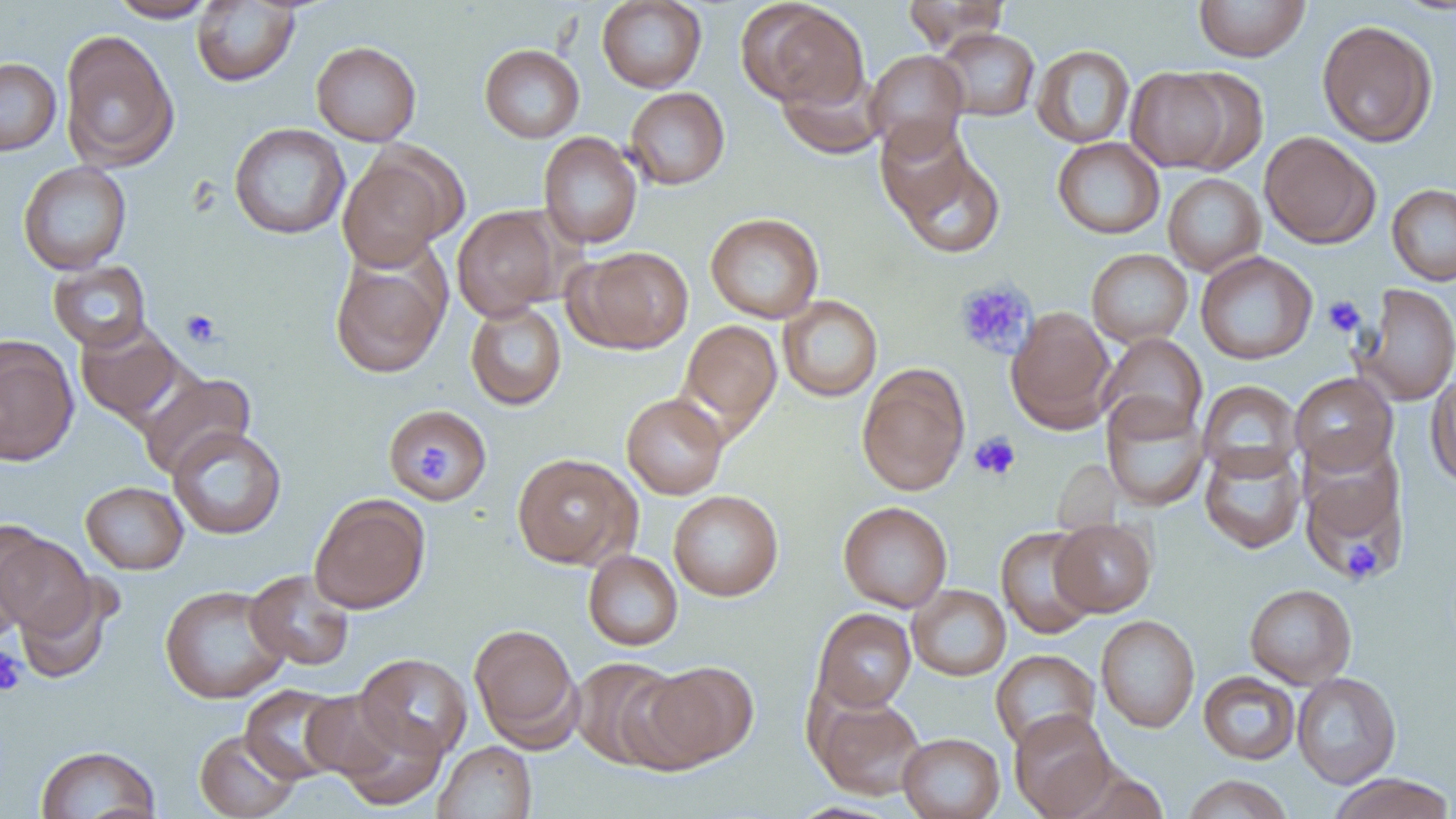
Approximate bounding boxes as [x1, y1, x2, y2] in pixels. Uninfected red blood cell locations: [108, 0, 219, 22], [597, 0, 707, 93], [902, 0, 1011, 52], [191, 1, 300, 87], [1193, 1, 1310, 61], [740, 2, 870, 111], [1316, 20, 1439, 147], [934, 27, 1040, 122], [59, 30, 180, 172], [311, 40, 421, 146], [479, 43, 585, 143], [1032, 45, 1135, 148], [864, 49, 968, 156], [0, 57, 62, 156], [1126, 66, 1239, 173], [777, 67, 885, 160], [624, 87, 730, 190], [229, 122, 350, 240], [1259, 131, 1380, 249], [538, 132, 642, 249], [1052, 137, 1165, 239], [887, 139, 1007, 262], [338, 148, 461, 271], [18, 161, 132, 275], [1163, 173, 1266, 276], [1387, 183, 1456, 286], [452, 205, 565, 320], [705, 212, 824, 324], [570, 245, 694, 354], [1086, 248, 1193, 346], [329, 251, 449, 380], [1196, 251, 1317, 364], [48, 261, 152, 353], [1354, 283, 1456, 405], [778, 295, 883, 402], [465, 301, 567, 410], [1006, 308, 1117, 432], [678, 320, 782, 435], [75, 321, 186, 426], [1098, 333, 1207, 439], [0, 337, 78, 466], [857, 366, 970, 496], [1426, 369, 1456, 489], [138, 372, 255, 479], [1290, 372, 1398, 476], [1197, 380, 1302, 481], [621, 393, 729, 500], [1101, 394, 1210, 512], [384, 404, 489, 505], [167, 426, 287, 540], [1199, 443, 1306, 553], [512, 453, 640, 569], [1300, 458, 1408, 584], [80, 481, 189, 574], [668, 490, 783, 601], [309, 493, 431, 614], [838, 501, 952, 612], [1050, 518, 1157, 616], [996, 527, 1099, 639], [0, 529, 96, 640], [583, 549, 683, 651], [244, 569, 355, 671], [14, 577, 119, 684], [159, 584, 290, 704], [907, 584, 1011, 681], [1244, 584, 1357, 689], [812, 608, 916, 712], [1096, 615, 1200, 732], [468, 622, 583, 750], [990, 649, 1100, 752], [354, 653, 473, 761], [569, 656, 688, 771], [636, 660, 758, 771], [1198, 671, 1300, 765], [1292, 672, 1401, 788], [239, 684, 351, 785], [300, 689, 407, 783], [812, 695, 927, 799], [331, 706, 447, 812], [1009, 709, 1116, 818], [194, 728, 302, 819], [898, 732, 1005, 819], [433, 741, 536, 819], [35, 745, 161, 819], [1327, 773, 1455, 819], [1181, 774, 1293, 819]. Platelet locations: [954, 278, 1038, 359], [1322, 296, 1366, 337], [179, 309, 221, 348], [969, 432, 1020, 480], [411, 440, 454, 485], [1342, 540, 1382, 582], [0, 648, 26, 697]. Slide-level diagnosis: no evidence of blood parasites. Image is 1456×819 pixels. Thin blood smear. Optical microscopy. 1000x magnification. Single field of view.